Name the parasite shown.
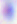
Toxoplasma gondii.

magnification = 400x
modality = photomicrograph